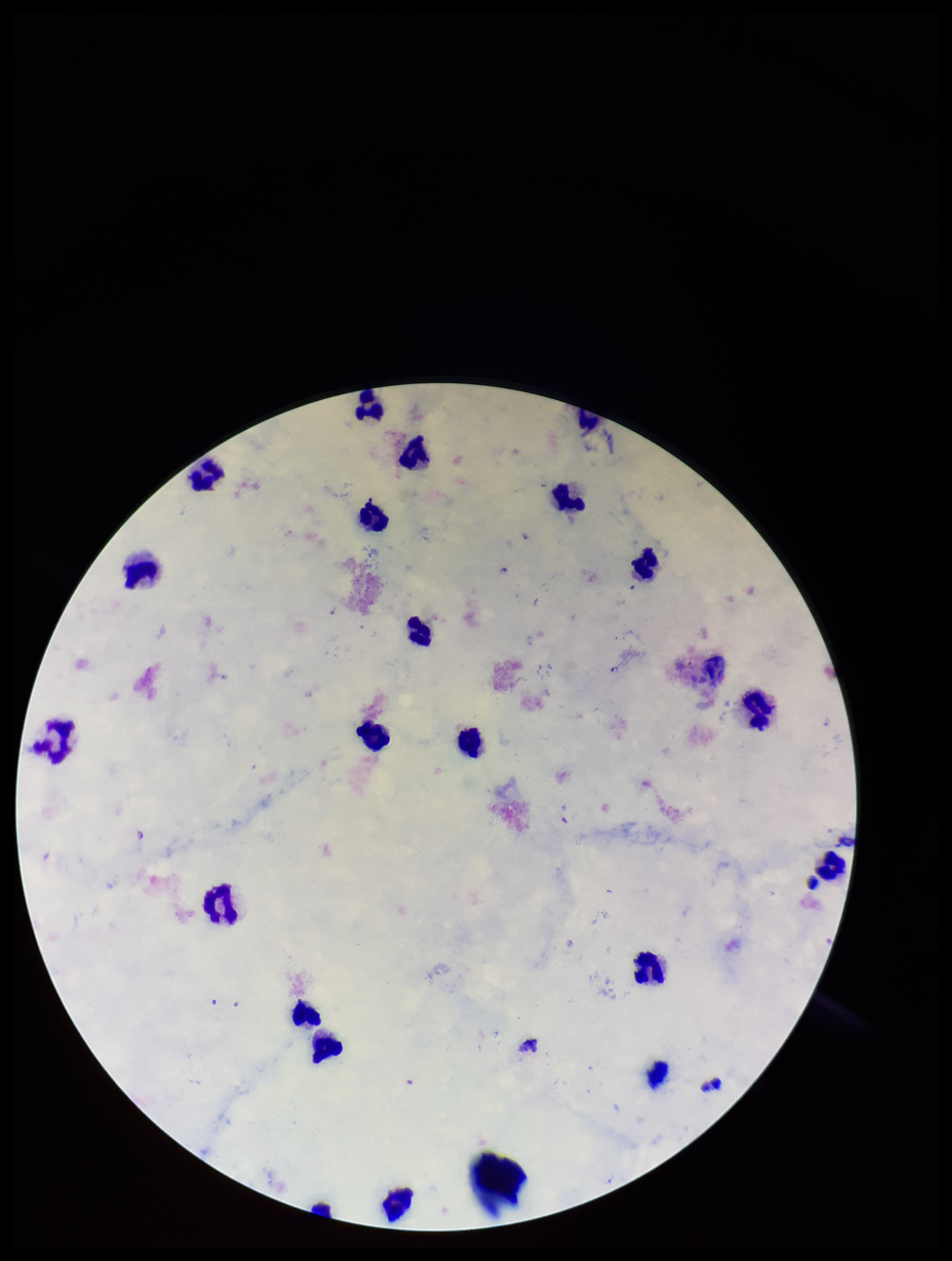 One field from this slide. Image is 952×1261 pixels. Leukocyte count: 22. Parasite count: 2. Giemsa stain. Preparation: thick smear. Smartphone photograph taken through the eyepiece of a microscope. Species reported for this patient: Plasmodium falciparum. Patient malaria status: positive. Plasmodium parasites: seen.